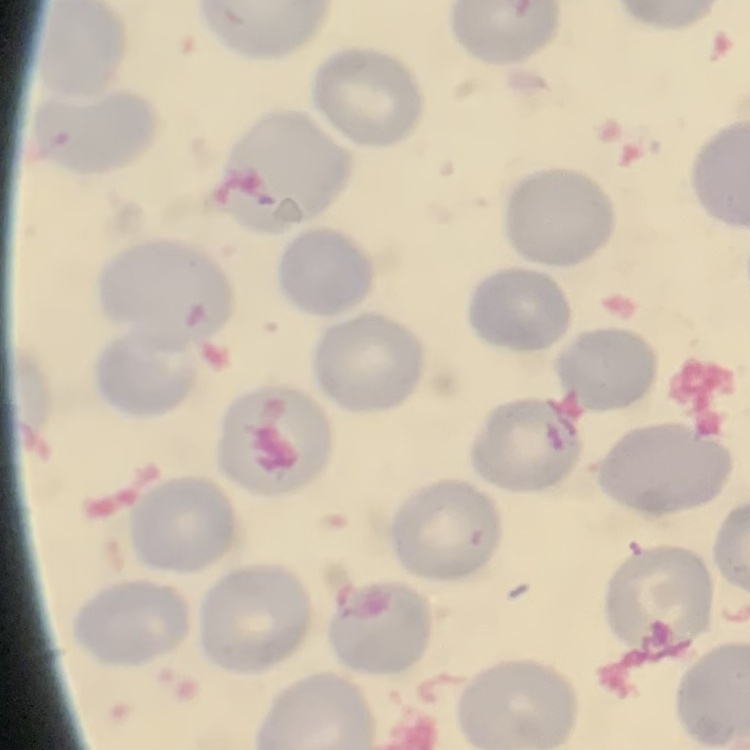

Summary:
  - Red blood cell morphology: no rouleaux formation
  - Stain: Field's or Giemsa
  - Image type: square crop of a larger photomicrograph
  - Preparation: thin blood smear